Evaluate for malaria.
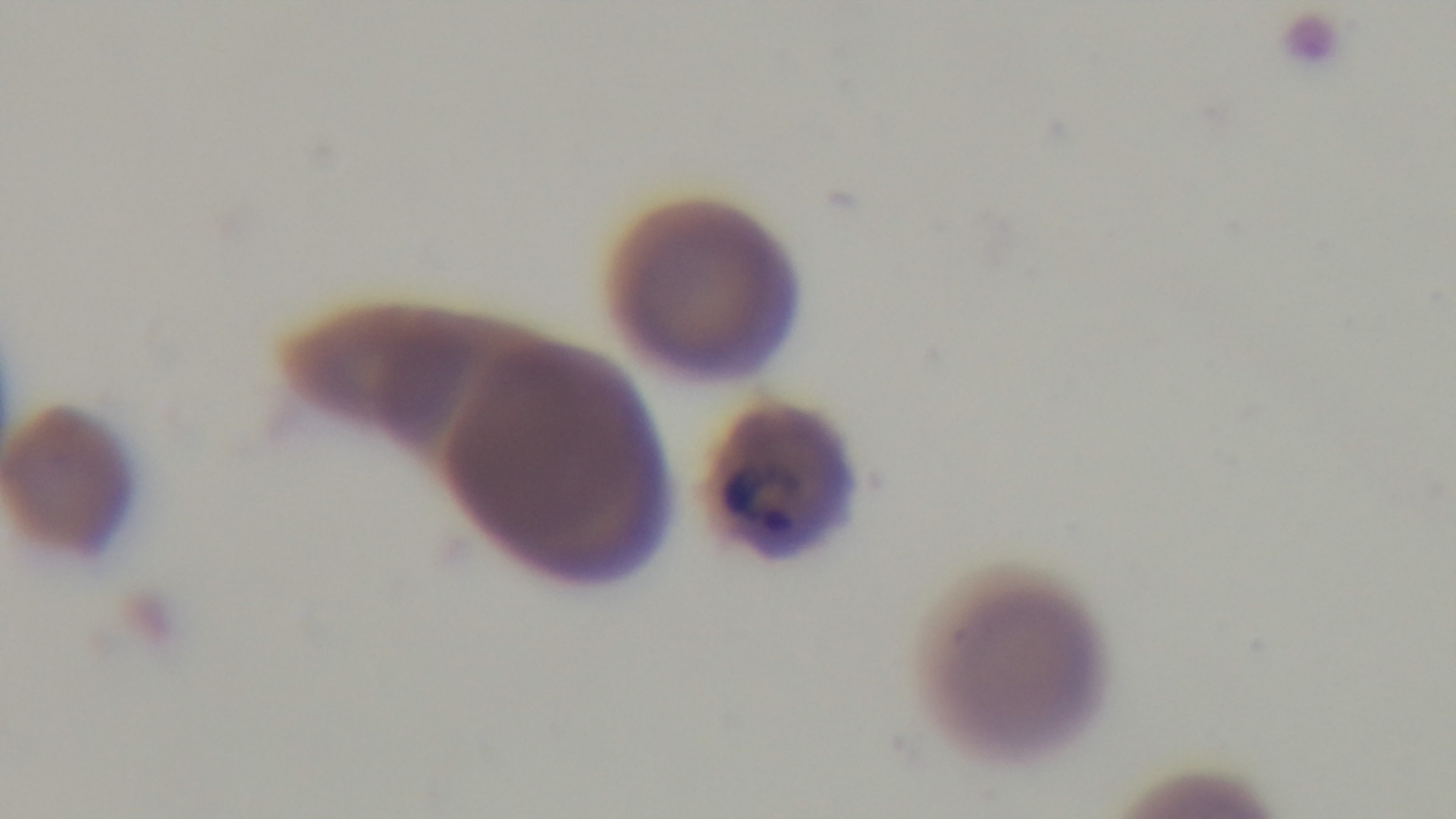

Infected.

Preparation: thin smear. Giemsa-stained. Single field of view. Photomicrograph. Oil-immersion objective, 100x. Captured with a mounted 4K digital camera.